Classify this cell by malaria status.
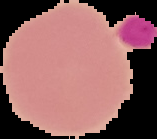
Uninfected.

image size = 157×139 pixels
image type = segmented cell region on a black background
preparation = thin blood film